State which parasite is depicted.
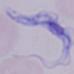

A trypanosome.

Summary:
  - Modality: photomicrograph
  - Magnification: 1000x